Describe the morphology of the red blood cells.
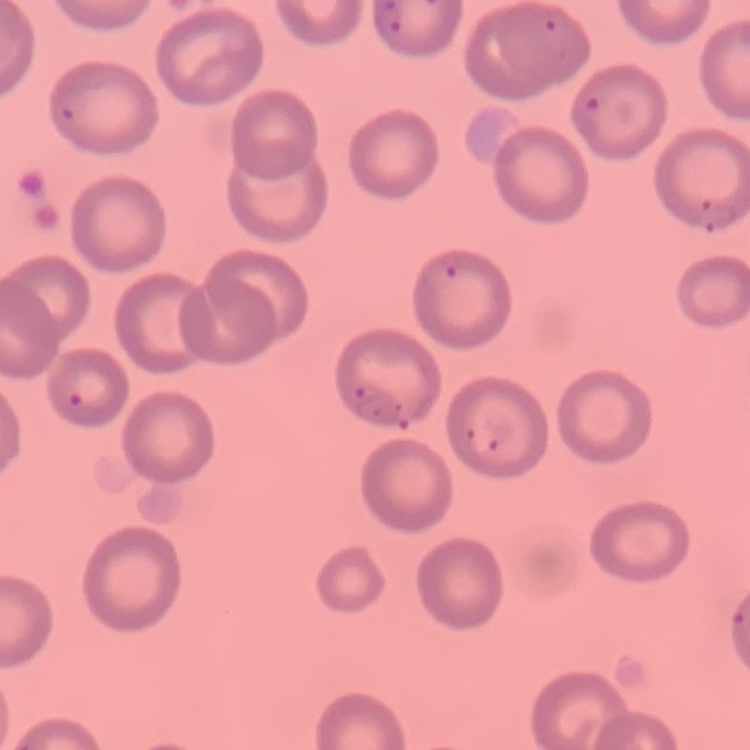
No rouleaux formation.

image type = one tile cut from a larger photomicrograph
stain = Field's or Giemsa
preparation = thin blood smear